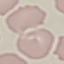

{
  "malaria_status": "uninfected",
  "preparation": "thin smear",
  "capture": "smartphone through the microscope eyepiece",
  "stain": "Giemsa",
  "image_type": "automatically extracted cell patch, resized to 64 × 64 pixels"
}